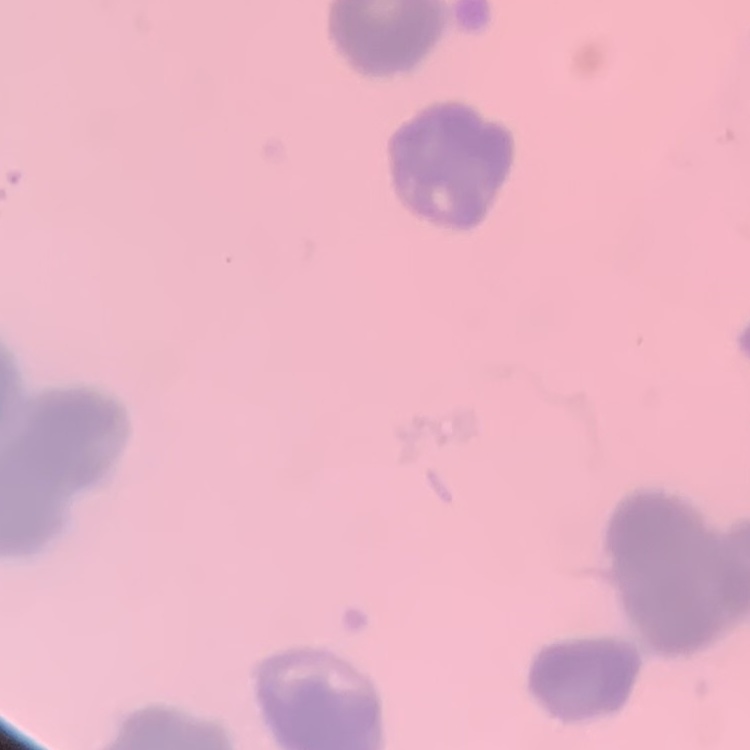

Summary:
  - Red blood cell morphology: rouleaux formation
  - Image type: one tile cut from a larger photomicrograph
  - Preparation: thin blood film
  - Stain: Field's or Giemsa